Classify this cell by malaria status.
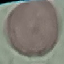

It is uninfected.

Photographed with a smartphone camera at the microscope eyepiece. Giemsa-stained preparation. Thin blood smear. Automatically extracted cell patch, resized to 64 × 64 pixels.